Describe the morphology of the red blood cells.
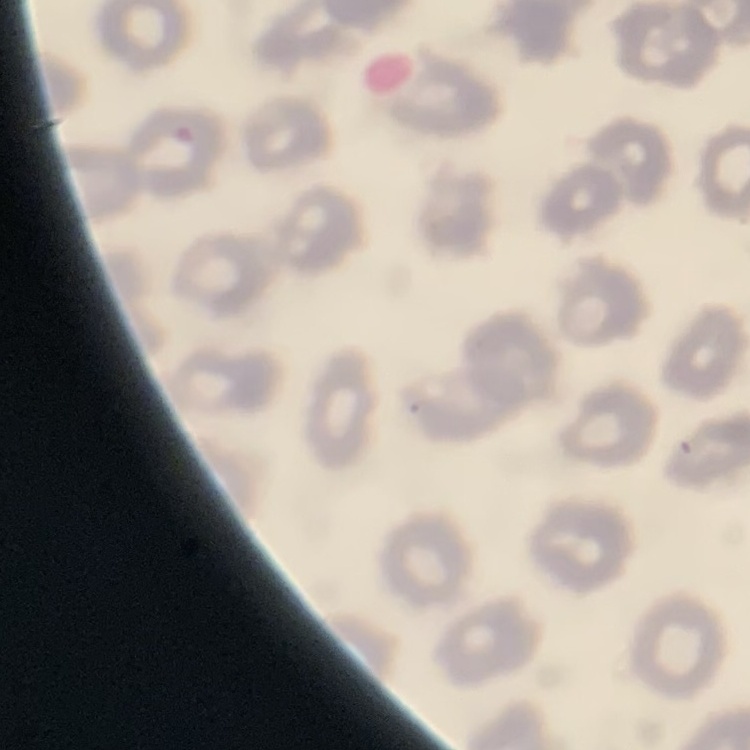
They show no rouleaux formation.

Thin peripheral smear. One tile cut from a larger photomicrograph. Stained with either Field's or Giemsa.